Assess this cell for malaria.
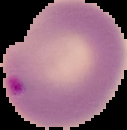

Parasitized.

Image is 127×130 pixels. The area outside the segmented cell region is set to black. From a thin blood film.